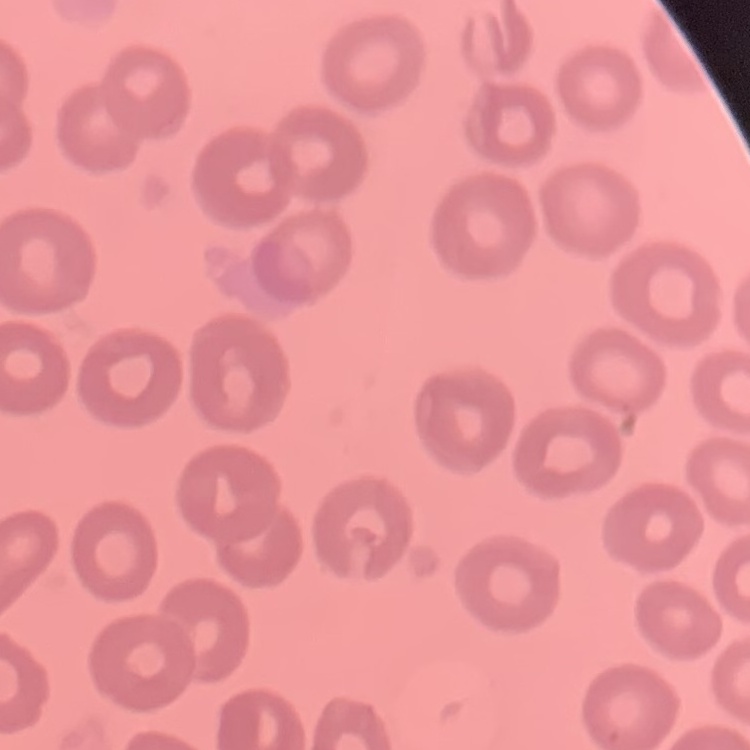
The red blood cells exhibit no rouleaux formation. Stained with either Field's or Giemsa. Thin blood smear. Square crop of a larger photomicrograph.